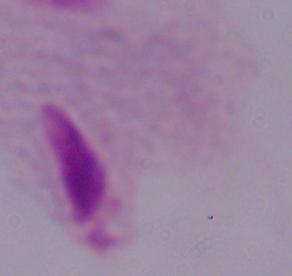

Summary:
  - Magnification: 1000x
  - Identification: trichomonad
  - Modality: photomicrograph